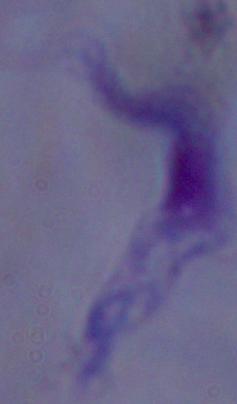

{
  "modality": "photomicrograph",
  "identification": "trypanosome",
  "magnification": "1000x"
}